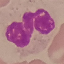

result = negative for malaria parasites
preparation = thin blood film
image type = cell patch, automatically extracted from a larger field of view and resized to 64 × 64 pixels
capture = smartphone camera at the microscope eyepiece
stain = Giemsa